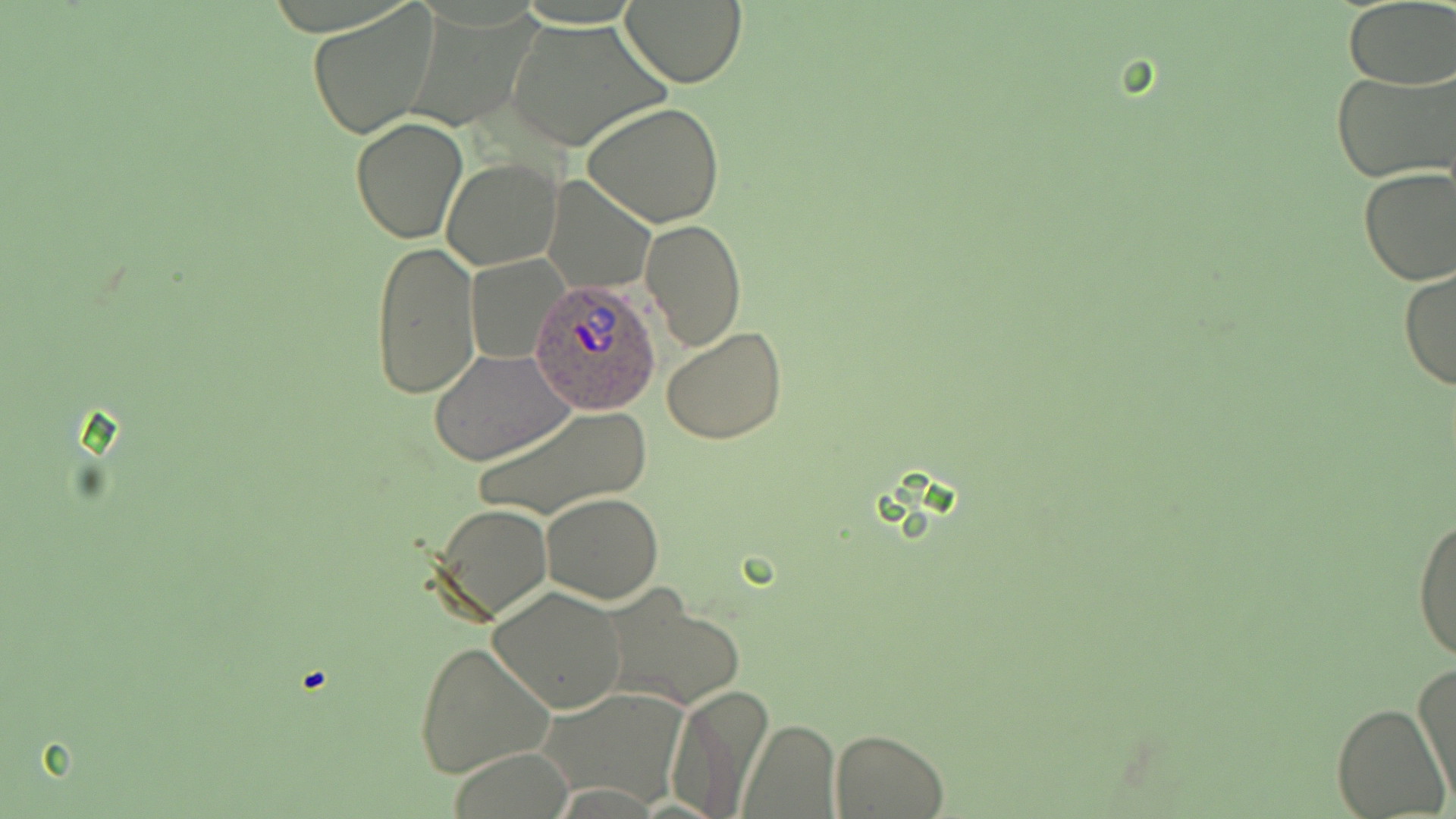

slide_level_diagnosis: Plasmodium ovale
stain: May-Grünwald-Giemsa
modality: optical microscopy
field_of_view: one of a larger specimen
plasmodium_ovale_infected_red_blood_cell_locations: 'approximate bounding boxes as named x1/y1/x2/y2 corners in pixels: (x1=531, y1=279, x2=661, y2=415)'
magnification: 1000x
image_size: 1456×819 pixels
preparation: thin blood film
uninfected_red_blood_cell_locations: 'approximate bounding boxes as named x1/y1/x2/y2 corners in pixels: (x1=619, y1=0, x2=746, y2=87), (x1=307, y1=2, x2=441, y2=140), (x1=1343, y1=3, x2=1456, y2=87), (x1=507, y1=20, x2=665, y2=154), (x1=1332, y1=68, x2=1456, y2=185), (x1=582, y1=101, x2=727, y2=229), (x1=350, y1=117, x2=467, y2=243), (x1=443, y1=159, x2=562, y2=270), (x1=1357, y1=168, x2=1456, y2=286), (x1=543, y1=176, x2=655, y2=292), (x1=640, y1=218, x2=747, y2=351), (x1=369, y1=240, x2=479, y2=400), (x1=467, y1=255, x2=568, y2=364), (x1=1398, y1=266, x2=1455, y2=391), (x1=661, y1=324, x2=786, y2=445), (x1=429, y1=348, x2=574, y2=466), (x1=472, y1=403, x2=652, y2=522), (x1=540, y1=493, x2=665, y2=603), (x1=431, y1=503, x2=554, y2=625), (x1=1411, y1=508, x2=1456, y2=667), (x1=487, y1=586, x2=627, y2=715), (x1=602, y1=587, x2=744, y2=713), (x1=412, y1=640, x2=556, y2=779), (x1=1413, y1=663, x2=1455, y2=803), (x1=662, y1=685, x2=771, y2=817), (x1=539, y1=688, x2=687, y2=807), (x1=1333, y1=703, x2=1450, y2=818), (x1=739, y1=721, x2=839, y2=816), (x1=831, y1=728, x2=948, y2=817)'